Outline each Trypanosoma brucei.
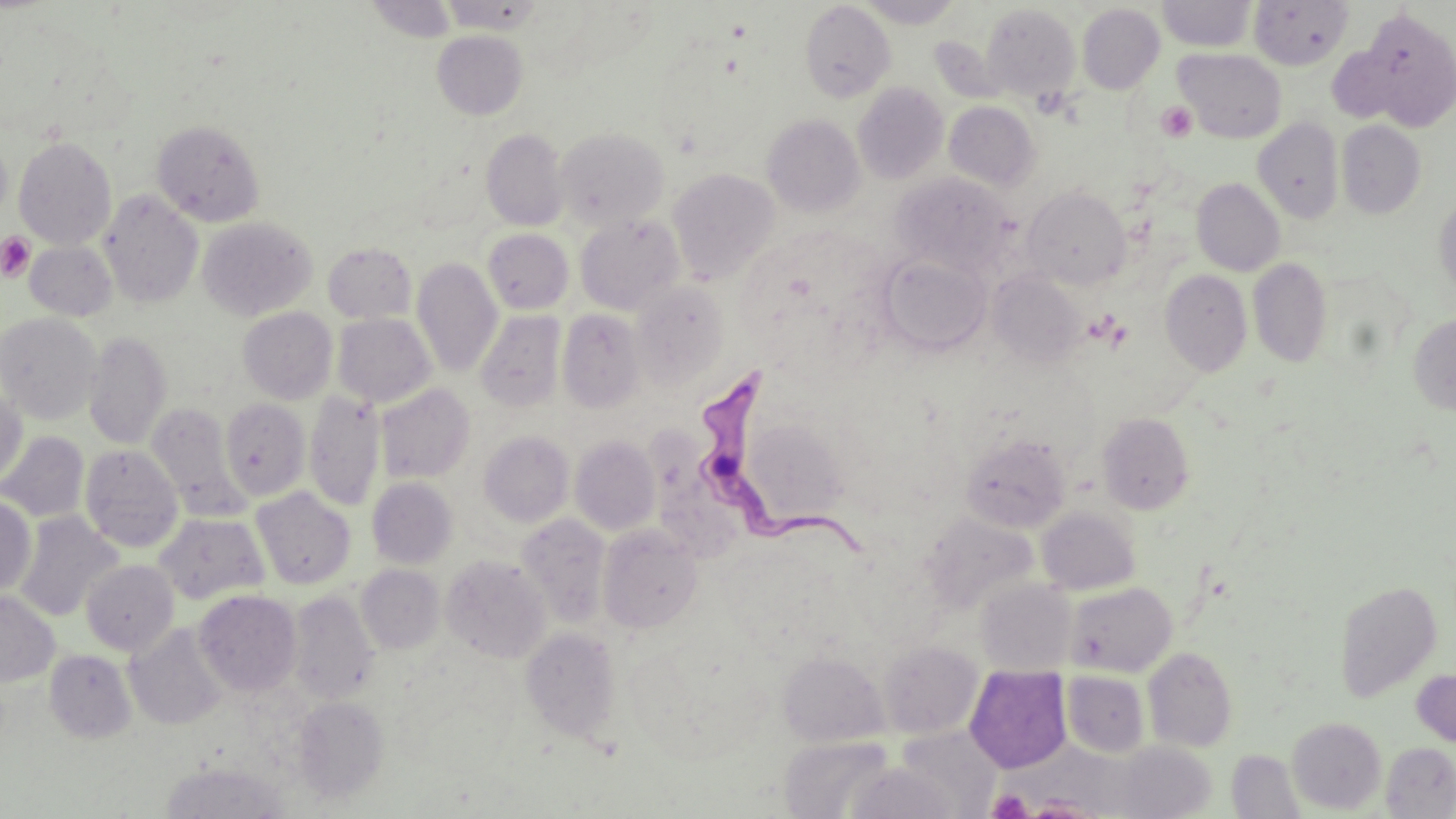

Approximate bounding boxes as (x1,y1)-(x2,y2) corner pairs in pixels.
Trypanosoma brucei: (701,371)-(865,560).

slide-level diagnosis = Trypanosoma brucei
stain = May-Grünwald-Giemsa
uninfected red blood cell locations = approximate bounding boxes as (x1,y1)-(x2,y2) corner pairs in pixels: (365,0)-(457,42), (439,0)-(546,33), (856,0)-(965,28), (1158,0)-(1256,52), (1249,0)-(1352,71), (800,2)-(896,103), (982,3)-(1081,101), (1077,3)-(1165,94), (1355,8)-(1456,129), (432,31)-(528,119), (1327,46)-(1404,124), (1175,48)-(1286,142), (853,83)-(948,184), (944,101)-(1040,191), (762,114)-(865,216), (1253,117)-(1344,224), (152,119)-(265,226), (1337,120)-(1426,219), (554,127)-(670,230), (481,129)-(569,231), (14,136)-(117,249), (0,137)-(12,224), (667,168)-(779,284), (891,172)-(1016,276), (1192,177)-(1285,276), (1022,186)-(1132,290), (99,190)-(203,308), (1434,194)-(1456,300), (575,213)-(685,314), (197,216)-(317,320), (483,228)-(574,314), (24,241)-(117,321), (323,242)-(417,324), (880,253)-(991,356), (412,257)-(502,377), (1248,257)-(1332,368), (1160,269)-(1252,377), (987,270)-(1086,369), (632,281)-(728,385), (239,307)-(337,404), (557,309)-(645,413), (475,311)-(566,412), (0,313)-(102,423), (332,313)-(435,407), (1408,314)-(1456,415), (83,331)-(171,449), (375,383)-(475,483), (0,387)-(27,487), (304,391)-(385,511), (220,397)-(311,500), (147,403)-(247,520), (1097,413)-(1195,515), (478,430)-(574,526), (0,431)-(90,523), (961,434)-(1071,532), (570,436)-(661,535), (80,444)-(183,552), (366,477)-(458,569), (251,487)-(356,590), (0,496)-(36,595), (1037,506)-(1140,595), (15,511)-(123,622), (154,512)-(269,606), (516,513)-(611,628), (921,513)-(1038,613), (598,525)-(703,634), (441,554)-(551,663), (81,559)-(179,656), (356,564)-(444,654), (975,579)-(1076,676), (1334,579)-(1442,702), (1064,581)-(1177,676), (0,590)-(60,686), (194,590)-(302,696), (286,590)-(380,704), (124,622)-(228,730), (520,626)-(622,744), (878,640)-(982,738), (1143,646)-(1238,752), (45,649)-(137,743), (778,651)-(889,746), (965,665)-(1071,773), (1411,668)-(1456,748), (1062,670)-(1150,758), (292,696)-(389,802), (1287,716)-(1387,814), (780,735)-(895,819), (1115,741)-(1216,819), (1381,742)-(1456,818), (1227,749)-(1305,818), (846,761)-(960,819)
platelet locations = approximate bounding boxes as (x1,y1)-(x2,y2) corner pairs in pixels: (1157,102)-(1198,142), (0,232)-(35,281), (987,788)-(1033,818)
magnification = 1000x
image size = 1456×819 pixels
modality = optical microscopy
preparation = thin blood smear
field of view = single